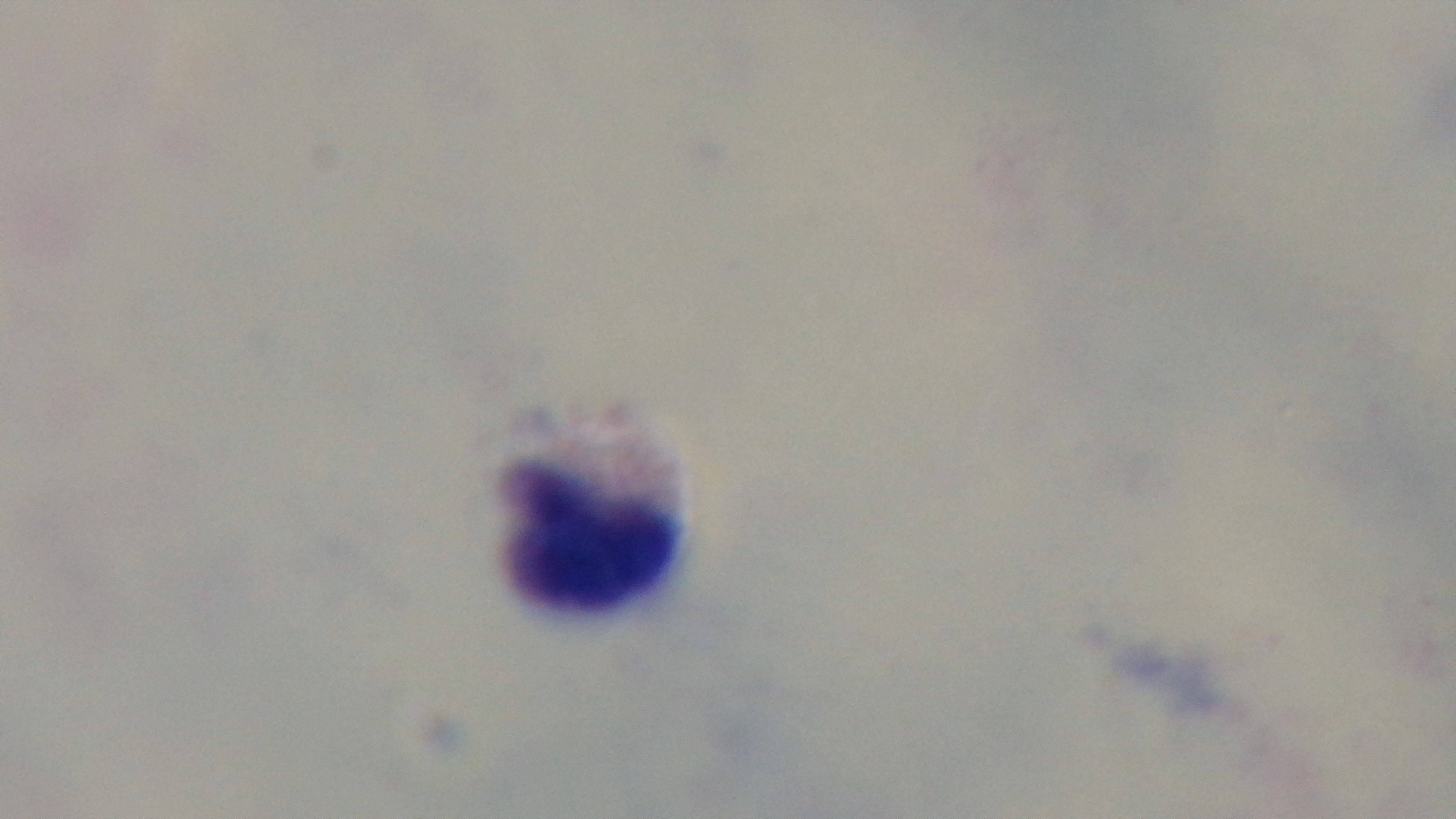

Preparation: thick blood film. One field from the slide. Oil-immersion objective, 100x. Photomicrograph. Malaria status: negative. Captured with a mounted 4K digital camera. Giemsa-stained.